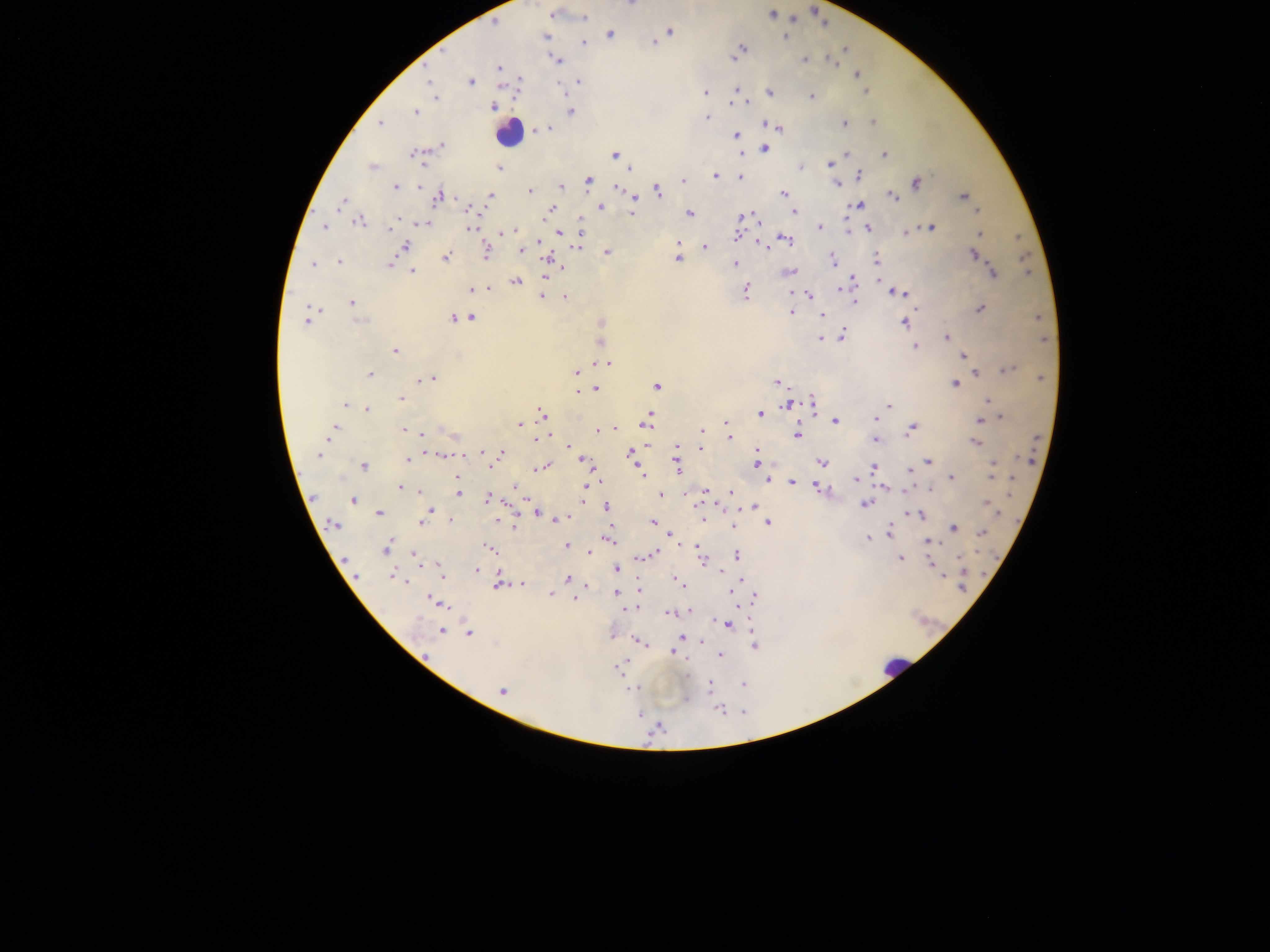
image size = 1270×952 pixels
preparation = thick blood smear
leukocyte locations = approximate centers as x y in pixels: 508 132; 894 667
malaria parasite locations = approximate centers as x y in pixels: 632 5; 554 13; 772 14; 583 18; 670 31; 609 33; 785 35; 545 36; 653 42; 582 43; 741 49; 844 50; 735 58; 804 58; 555 59; 830 60; 499 67; 856 73; 520 80; 428 82; 470 82; 578 82; 518 84; 736 90; 866 91; 704 92; 769 92; 435 97; 811 97; 746 102; 731 103; 494 106; 570 111; 415 112; 707 117; 844 122; 872 122; 379 123; 764 124; 548 128; 780 128; 540 129; 537 132; 735 135; 441 146; 764 148; 846 153; 414 154; 613 154; 883 154; 421 158; 423 164; 829 164; 373 167; 498 167; 800 168; 630 170; 715 175; 858 175; 740 177; 683 180; 588 181; 915 182; 836 183; 417 184; 394 187; 559 187; 615 187; 529 191; 658 191; 783 194; 489 195; 637 195; 963 195; 438 196; 893 196; 341 203; 633 203; 858 204; 600 207; 466 208; 549 208; 978 209; 793 211; 632 212; 689 213; 847 215; 396 216; 741 217; 358 221; 580 222; 422 223; 325 226; 820 226; 845 227; 930 227; 389 228; 470 228; 869 228; 505 232; 905 232; 559 233; 581 233; 847 233; 979 233; 737 236; 783 238; 540 240; 677 242; 762 244; 539 245; 405 246; 703 247; 518 249; 485 251; 606 251; 973 254; 445 257; 678 257; 876 259; 833 261; 338 262; 389 263; 734 264; 313 265; 561 267; 789 271; 412 272; 992 273; 1028 274; 545 277; 877 278; 515 281; 853 282; 471 289; 488 289; 837 289; 745 290; 898 292; 790 293; 809 295; 541 296; 565 297; 854 302; 351 303; 309 307; 979 308; 789 312; 822 314; 471 317; 1037 317; 453 318; 306 321; 359 321; 599 322; 904 322; 840 334; 825 337; 947 337; 820 338; 1044 339; 598 343; 915 346; 394 351; 963 355; 608 363; 1008 368; 576 373; 975 373; 368 375; 431 378; 1041 378; 776 382; 954 384; 657 385; 595 388; 576 391; 401 398; 812 400; 987 400; 345 405; 787 405; 887 406; 367 409; 811 409; 761 413; 541 414; 999 416; 875 418; 646 420; 835 421; 979 421; 519 424; 726 424; 334 427; 615 428; 912 429; 401 430; 598 430; 701 431; 331 432; 796 433; 422 434; 730 438; 535 439; 875 440; 975 441; 646 446; 568 447; 676 447; 700 448; 757 450; 484 453; 629 453; 439 454; 502 454; 319 455; 463 455; 675 457; 407 460; 585 461; 927 461; 821 462; 589 463; 757 463; 993 463; 363 465; 544 467; 873 467; 677 468; 908 472; 640 474; 458 478; 855 478; 950 478; 991 478; 1012 480; 768 481; 791 482; 514 487; 401 488; 584 488; 818 489; 886 489; 419 491; 704 491; 731 491; 1011 493; 457 494; 582 494; 660 494; 312 497; 487 498; 352 500; 587 502; 864 503; 987 503; 722 506; 753 506; 607 507; 430 511; 378 513; 535 513; 996 513; 913 514; 427 515; 552 517; 558 517; 701 519; 422 520; 653 522; 767 522; 333 526; 516 527; 732 527; 954 527; 888 533; 670 535; 980 535; 868 537; 609 539; 928 541; 566 545; 696 545; 385 549; 490 549; 589 551; 698 551; 654 553; 736 554; 414 556; 900 558; 959 558; 702 560; 346 563; 930 564; 616 568; 475 570; 441 572; 942 574; 394 576; 567 578; 740 578; 407 580; 679 581; 521 583; 585 583; 498 584; 637 590; 731 592; 550 593; 615 593; 754 597; 575 598; 436 602; 735 605; 634 606; 628 608; 690 612; 669 613; 727 625; 440 630; 751 630; 468 633; 613 636; 680 639; 639 641; 701 641; 645 643; 754 646; 673 651; 720 656; 617 669; 686 675; 742 685; 708 686; 629 688; 502 691; 719 708
field of view = single
capture = mobile-phone photograph through a microscope
country = Ghana